Assess this cell for malaria.
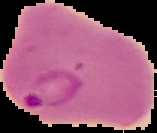

Parasitized.

Segmented cell region on a black background. From a thin blood film. Image is 157×133 pixels.